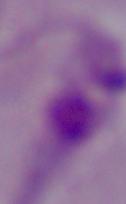

Summary:
  - Identification: Leishmania
  - Magnification: 1000x
  - Modality: micrograph